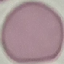

Summary:
  - Result: no malaria parasites detected
  - Preparation: thin blood smear
  - Stain: Giemsa
  - Image type: cell patch, automatically extracted from a larger field of view and resized to 64 × 64 pixels
  - Capture: smartphone camera at the microscope eyepiece